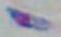
identification: Toxoplasma gondii
magnification: 1000x
modality: micrograph